Report the malaria status of this cell.
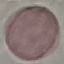

Uninfected.

preparation = thin blood smear
stain = Giemsa
capture = smartphone camera at the microscope eyepiece
image type = automatically extracted cell patch, resized to 64 × 64 pixels